Outline each Plasmodium malariae-infected red blood cell.
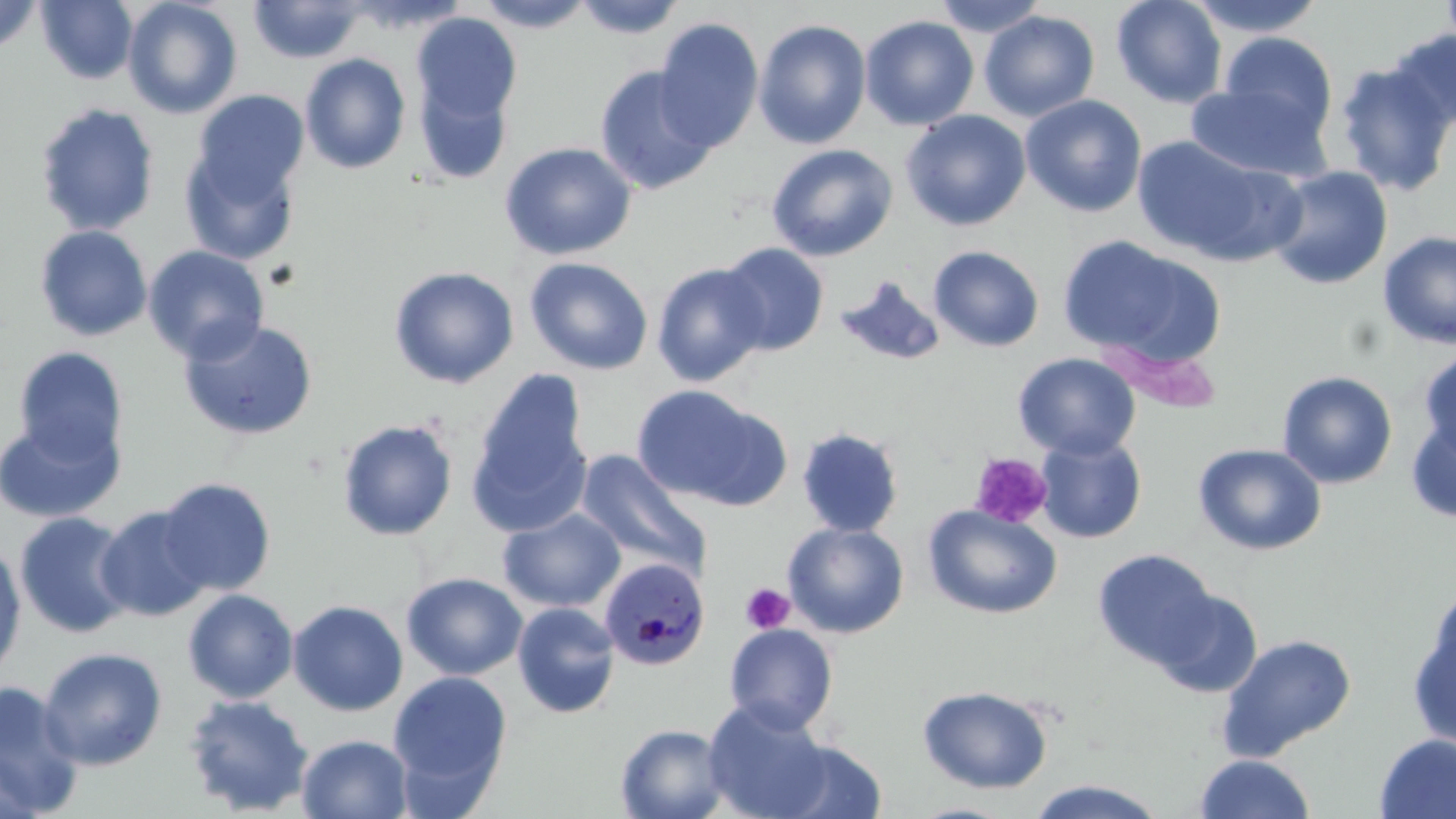
Approximate bounding boxes as [x1, y1, x2, y2] in pixels.
Plasmodium malariae-infected red blood cells: [598, 556, 711, 671].

slide-level diagnosis = Plasmodium malariae
platelet locations = approximate bounding boxes as [x1, y1, x2, y2] in pixels: [970, 453, 1052, 529], [740, 583, 795, 634]
stain = May-Grünwald-Giemsa
modality = optical microscopy
preparation = thin blood film
image size = 1456×819 pixels
uninfected red blood cell locations = approximate bounding boxes as [x1, y1, x2, y2] in pixels: [36, 0, 138, 85], [122, 0, 243, 119], [474, 0, 596, 32], [571, 0, 688, 39], [931, 0, 1051, 37], [1111, 0, 1228, 108], [1185, 0, 1328, 37], [1439, 0, 1456, 60], [0, 1, 42, 54], [248, 1, 366, 64], [979, 10, 1100, 122], [412, 13, 522, 123], [859, 15, 980, 131], [653, 17, 764, 152], [753, 18, 872, 149], [1385, 28, 1456, 131], [1217, 31, 1340, 144], [300, 53, 411, 173], [1334, 60, 1456, 196], [594, 65, 717, 195], [413, 75, 513, 185], [1186, 82, 1333, 183], [192, 90, 309, 201], [1020, 94, 1147, 217], [35, 103, 160, 236], [900, 110, 1031, 231], [1130, 135, 1292, 265], [499, 141, 637, 261], [766, 143, 899, 262], [180, 145, 301, 265], [1267, 166, 1394, 290], [34, 225, 152, 341], [1378, 230, 1456, 349], [1056, 235, 1211, 363], [717, 242, 830, 356], [142, 245, 270, 365], [928, 245, 1045, 352], [524, 256, 653, 375], [651, 262, 770, 387], [389, 266, 520, 389], [834, 275, 946, 368], [179, 318, 319, 441], [13, 346, 129, 463], [1417, 346, 1456, 462], [1012, 352, 1140, 460], [466, 369, 594, 537], [1276, 370, 1398, 489], [631, 384, 782, 508], [1405, 412, 1456, 524], [0, 414, 124, 523], [337, 419, 458, 541], [796, 426, 905, 538], [1034, 434, 1148, 544], [1192, 443, 1327, 555], [575, 452, 710, 579], [156, 477, 276, 597], [95, 504, 214, 623], [922, 505, 1063, 619], [498, 507, 625, 613], [13, 511, 135, 639], [782, 521, 909, 638], [0, 542, 27, 683], [1092, 548, 1220, 671], [401, 572, 527, 680], [1424, 583, 1456, 692], [1150, 587, 1263, 698], [182, 589, 299, 704], [287, 599, 409, 716], [512, 602, 621, 718], [1407, 606, 1456, 751], [724, 623, 839, 735], [1216, 632, 1358, 762], [38, 646, 168, 771], [388, 671, 512, 798], [0, 681, 86, 817], [917, 685, 1054, 794], [183, 694, 314, 816], [702, 699, 834, 819], [615, 723, 732, 819], [1374, 733, 1456, 819], [297, 734, 413, 819], [771, 738, 888, 819], [0, 749, 42, 819], [1193, 754, 1317, 819], [1023, 779, 1170, 818]
magnification = 1000x
field of view = single